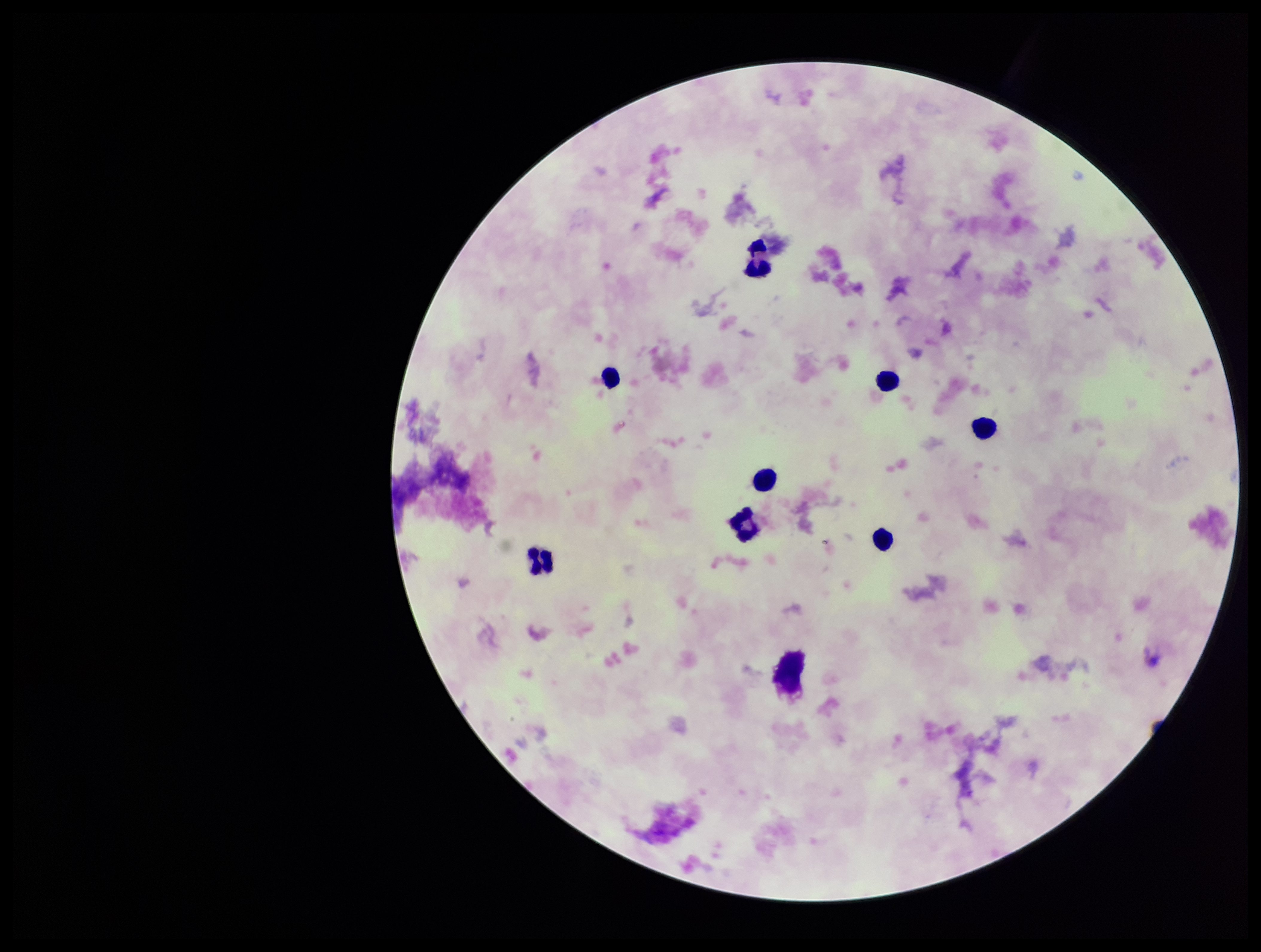

leukocyte count = 9
patient malaria status = negative
image size = 1261×952 pixels
preparation = thick
Plasmodium parasites = none identified
stain = Giemsa
field of view = single
capture = smartphone photograph through the microscope eyepiece
parasite count = 0